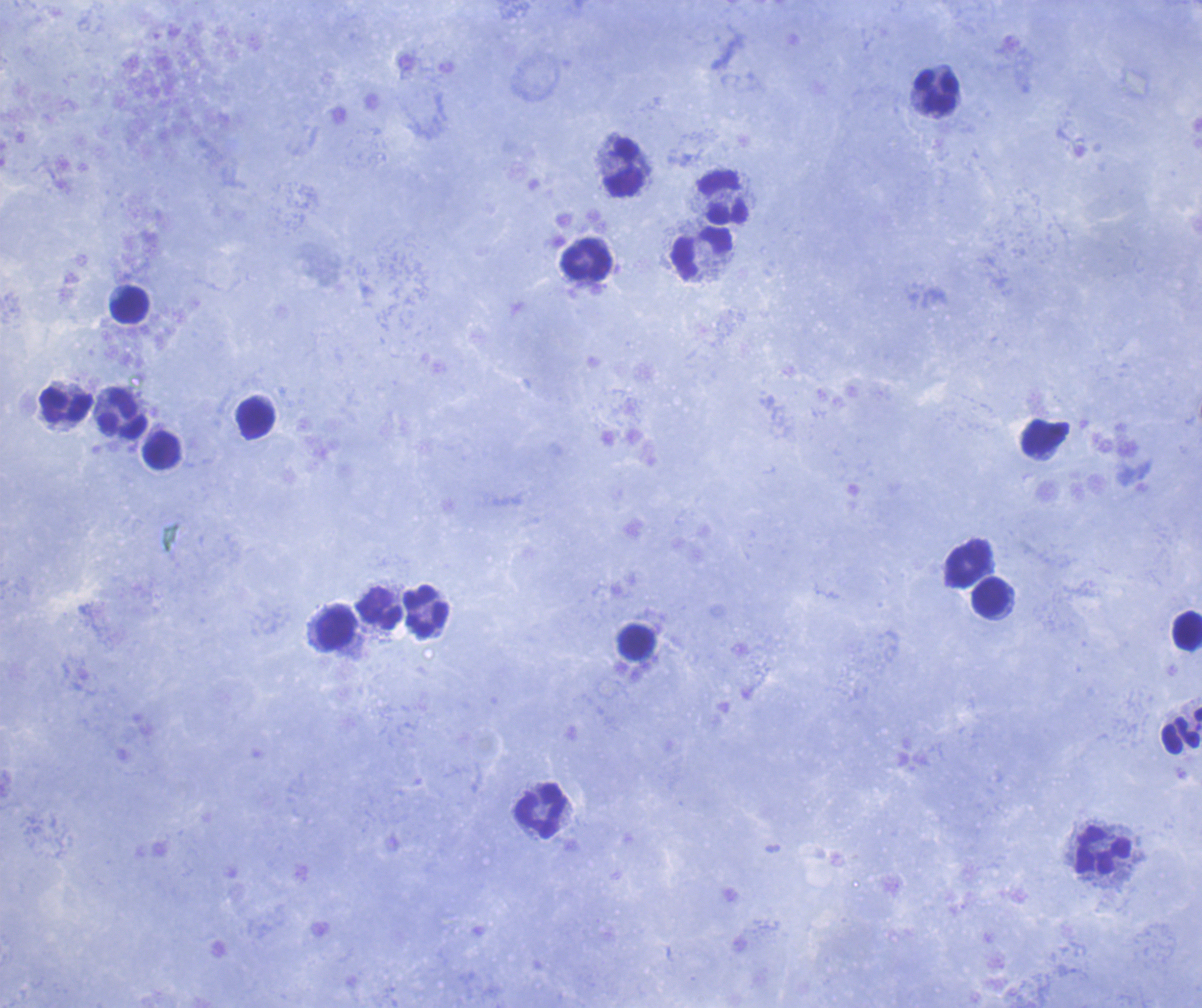
Approximate object centers, in pixels from the top-left corner.
Summary:
  - Leukocyte locations: (x=939, y=93), (x=625, y=169), (x=724, y=198), (x=703, y=254), (x=587, y=259), (x=130, y=305), (x=67, y=404), (x=123, y=411), (x=256, y=418), (x=1046, y=436), (x=162, y=450), (x=968, y=562), (x=991, y=597), (x=380, y=610), (x=425, y=611), (x=336, y=628), (x=1187, y=631), (x=636, y=641), (x=1181, y=730), (x=541, y=810), (x=1101, y=849)
  - Preparation: thick smear of blood
  - Context: previously used in a real diagnosis
  - Stain: Romanowsky
  - Result: negative for Plasmodium parasites
  - Field of view: single
  - Background quality: satisfactory
  - Coloration quality: good
  - Image size: 1202×1008 pixels
  - Magnification: 100x